Outline each blood parasite and name the species.
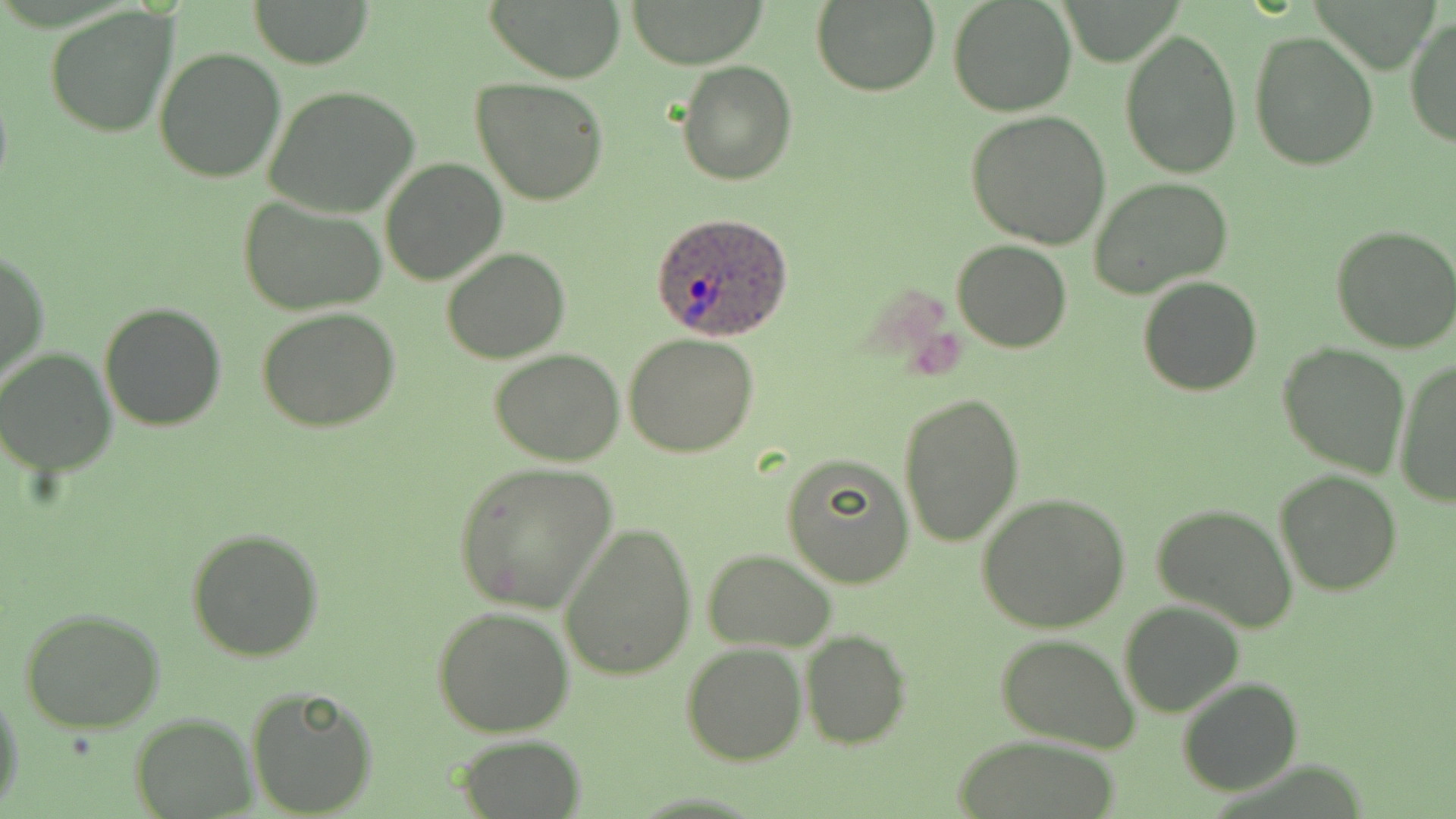

Approximate bounding boxes as (x1, y1, x2, y2) in pixels.
Plasmodium ovale-infected red blood cells: (651, 210, 796, 341).
No Plasmodium falciparum, Plasmodium malariae, Plasmodium vivax, Babesia divergens, or Trypanosoma brucei observed.

Summary:
  - Uninfected red blood cell locations: (247, 0, 375, 68), (488, 0, 626, 82), (623, 0, 772, 68), (811, 0, 941, 97), (949, 0, 1075, 116), (46, 5, 179, 138), (1404, 15, 1455, 149), (1120, 30, 1242, 178), (1249, 32, 1380, 172), (153, 46, 286, 183), (677, 61, 797, 185), (470, 78, 609, 207), (262, 86, 420, 217), (968, 109, 1111, 249), (380, 158, 506, 284), (1089, 177, 1233, 298), (237, 197, 387, 317), (1332, 225, 1456, 352), (952, 239, 1072, 353), (441, 247, 571, 364), (1, 249, 48, 386), (1137, 274, 1263, 396), (99, 302, 228, 431), (256, 306, 401, 434), (625, 333, 760, 458), (1277, 342, 1408, 477), (0, 348, 117, 477), (489, 348, 626, 465), (1392, 359, 1456, 507), (897, 391, 1024, 548), (781, 454, 915, 588), (453, 463, 616, 613), (1274, 469, 1402, 595), (977, 492, 1133, 635), (1152, 500, 1299, 631), (560, 523, 698, 680), (185, 527, 327, 664), (703, 549, 838, 652), (1120, 601, 1246, 717), (431, 605, 574, 739), (19, 607, 166, 735), (801, 630, 911, 748), (995, 634, 1140, 752), (681, 642, 808, 767), (1177, 677, 1303, 796), (245, 686, 380, 817), (0, 689, 22, 808), (131, 713, 254, 817), (453, 735, 588, 817), (950, 736, 1126, 819)
  - Slide-level diagnosis: Plasmodium ovale
  - Preparation: thin blood film
  - Image size: 1456×819 pixels
  - Modality: optical microscopy
  - Magnification: 1000x
  - Stain: May-Grünwald-Giemsa
  - Field of view: single